Identify the parasite.
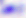
This is Toxoplasma gondii.

Photomicrograph. 400x magnification.